State the blood parasite species.
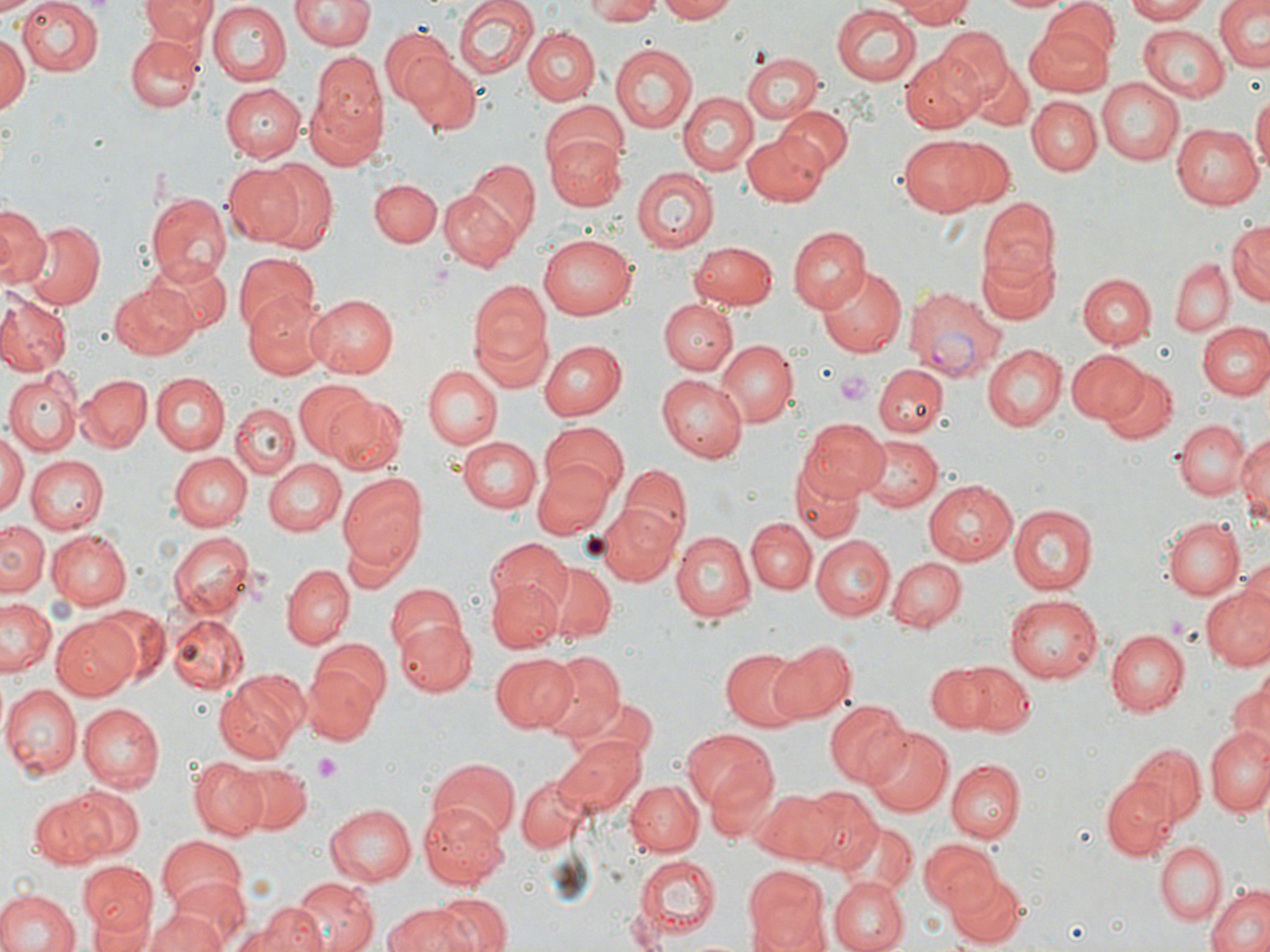
Plasmodium vivax.

preparation = thin blood film
magnification = 1000x
platelet locations = approximate bounding boxes as (x1, y1, x2, y2) in pixels: (836, 371, 873, 405), (314, 754, 342, 780)
Plasmodium vivax-infected red blood cell locations = approximate bounding boxes as (x1, y1, x2, y2) in pixels: (904, 287, 1006, 383)
uninfected red blood cell locations = approximate bounding boxes as (x1, y1, x2, y2) in pixels: (0, 0, 43, 18), (15, 0, 101, 76), (140, 0, 216, 47), (293, 0, 372, 52), (454, 0, 537, 81), (586, 0, 663, 24), (652, 0, 739, 23), (888, 0, 978, 26), (997, 0, 1073, 14), (1123, 0, 1212, 22), (1214, 0, 1270, 72), (206, 2, 291, 85), (1043, 4, 1120, 70), (831, 6, 923, 85), (1024, 21, 1116, 96), (1138, 24, 1230, 102), (934, 26, 1014, 106), (380, 27, 459, 109), (522, 27, 600, 107), (0, 32, 29, 118), (126, 35, 203, 112), (611, 42, 697, 134), (900, 49, 986, 132), (741, 52, 823, 124), (307, 55, 387, 166), (407, 57, 480, 134), (969, 65, 1033, 129), (1095, 79, 1184, 166), (218, 83, 305, 161), (679, 91, 758, 176), (1251, 91, 1270, 176), (1027, 95, 1100, 174), (537, 101, 627, 179), (776, 106, 853, 174), (1169, 121, 1264, 210), (544, 126, 624, 210), (742, 128, 833, 204), (899, 136, 986, 215), (942, 137, 1017, 208), (462, 160, 541, 245), (255, 161, 337, 250), (222, 162, 303, 245), (632, 167, 718, 253), (369, 177, 441, 249), (439, 186, 523, 270), (149, 192, 232, 281), (978, 197, 1058, 285), (0, 207, 46, 289), (1227, 220, 1269, 308), (23, 222, 107, 309), (788, 225, 868, 312), (536, 233, 635, 321), (690, 240, 779, 308), (977, 250, 1059, 325), (233, 253, 321, 337), (143, 258, 232, 332), (1171, 258, 1232, 336), (1176, 260, 1255, 380), (817, 265, 906, 357), (1077, 268, 1230, 340), (1078, 274, 1156, 348), (110, 281, 202, 360), (471, 281, 552, 386), (0, 291, 144, 370), (306, 294, 399, 378), (0, 296, 71, 374), (242, 297, 330, 381), (659, 299, 737, 375), (1187, 310, 1267, 465), (1197, 321, 1269, 399), (539, 340, 626, 421), (715, 341, 795, 426), (981, 344, 1066, 431), (1066, 349, 1146, 423), (425, 364, 503, 448), (875, 364, 945, 438), (1100, 367, 1179, 445), (5, 372, 81, 454), (78, 374, 152, 452), (153, 374, 229, 455), (658, 374, 747, 464), (295, 379, 375, 459), (326, 396, 406, 478), (232, 403, 297, 479), (801, 418, 891, 499), (1173, 418, 1251, 500), (538, 420, 628, 501), (1235, 427, 1270, 528), (0, 431, 25, 518), (458, 435, 541, 511), (859, 435, 942, 514), (170, 451, 252, 529), (26, 456, 108, 534), (265, 459, 346, 535), (621, 463, 692, 546), (531, 464, 616, 537), (789, 464, 865, 541), (339, 474, 428, 567), (923, 479, 1019, 566), (591, 501, 681, 585), (1008, 503, 1098, 597), (747, 517, 817, 593), (1161, 517, 1244, 600), (0, 520, 48, 596), (46, 529, 131, 609), (169, 531, 254, 622), (671, 531, 756, 623), (810, 534, 894, 620), (488, 536, 572, 618), (340, 537, 402, 593), (887, 557, 965, 629), (281, 563, 354, 646), (546, 564, 617, 643), (486, 575, 563, 653), (384, 582, 467, 659), (1202, 584, 1270, 672), (1005, 592, 1104, 681), (2, 597, 59, 677), (98, 604, 169, 683), (51, 614, 140, 700), (165, 614, 249, 694), (393, 620, 476, 695), (1105, 629, 1190, 715), (767, 638, 854, 723), (719, 648, 808, 731), (536, 651, 625, 742), (489, 652, 579, 732), (304, 654, 388, 741), (951, 661, 1037, 735), (924, 663, 1002, 731), (215, 672, 303, 762), (1227, 678, 1269, 752), (1, 684, 81, 776), (825, 700, 909, 788), (75, 704, 162, 791), (1206, 726, 1270, 816), (864, 727, 953, 816), (680, 729, 779, 815), (554, 735, 646, 814), (1127, 743, 1206, 829), (190, 758, 269, 839), (424, 758, 518, 840), (944, 758, 1024, 843), (231, 760, 312, 835), (515, 772, 592, 855), (1100, 779, 1176, 861), (625, 780, 700, 856), (66, 787, 141, 858), (750, 787, 836, 863), (800, 787, 881, 867), (30, 793, 108, 867), (421, 800, 507, 888), (325, 803, 417, 884), (843, 822, 917, 892), (156, 837, 245, 918), (921, 838, 999, 911), (1156, 840, 1226, 925), (632, 853, 720, 943), (78, 861, 159, 940), (743, 867, 829, 952), (947, 874, 1027, 945), (161, 878, 247, 949), (291, 878, 379, 952), (829, 878, 905, 952), (1205, 885, 1270, 952), (0, 888, 78, 952), (431, 893, 512, 952), (86, 903, 155, 952), (141, 904, 230, 951), (385, 904, 478, 952), (246, 906, 322, 951)
field of view = single
modality = optical microscopy
stain = May-Grünwald-Giemsa
image size = 1270×952 pixels